Report the malaria status of this cell.
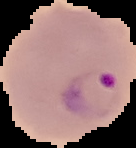

Parasitized.

preparation: thin blood film
image_size: 136×148 pixels
image_type: segmented cell region with the area outside set to black